Give the extent of all Plasmodium parasites.
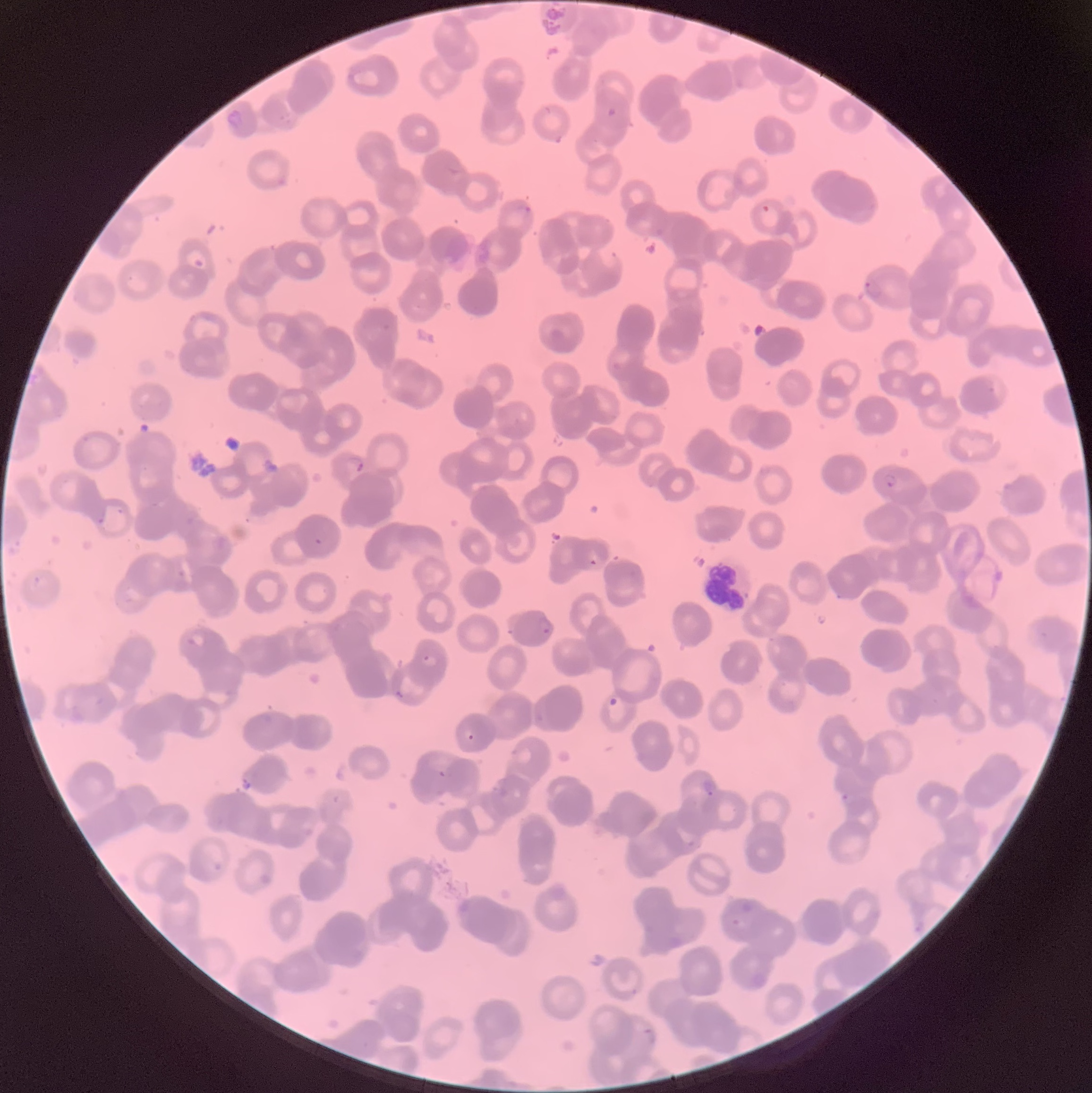
Approximate bounding boxes as (x1,y1)-(x2,y2) corner pairs in pixels.
Plasmodium parasites: (606,106)-(618,120), (515,203)-(532,216), (760,203)-(772,213), (863,278)-(884,300), (348,454)-(366,472), (883,472)-(898,489), (94,516)-(107,528), (313,526)-(329,545), (587,558)-(599,567), (537,615)-(554,637), (185,632)-(207,649), (421,652)-(438,668), (393,689)-(410,702), (608,696)-(619,708), (464,730)-(476,742), (437,768)-(448,779), (700,777)-(717,797), (841,792)-(854,804), (643,1026)-(657,1045).

Summary:
  - Modality: optical microscopy
  - Red blood cell morphology: rouleaux formation
  - Image size: 1092×1093 pixels
  - Preparation: thin blood film